Comment on the morphology of the erythrocytes.
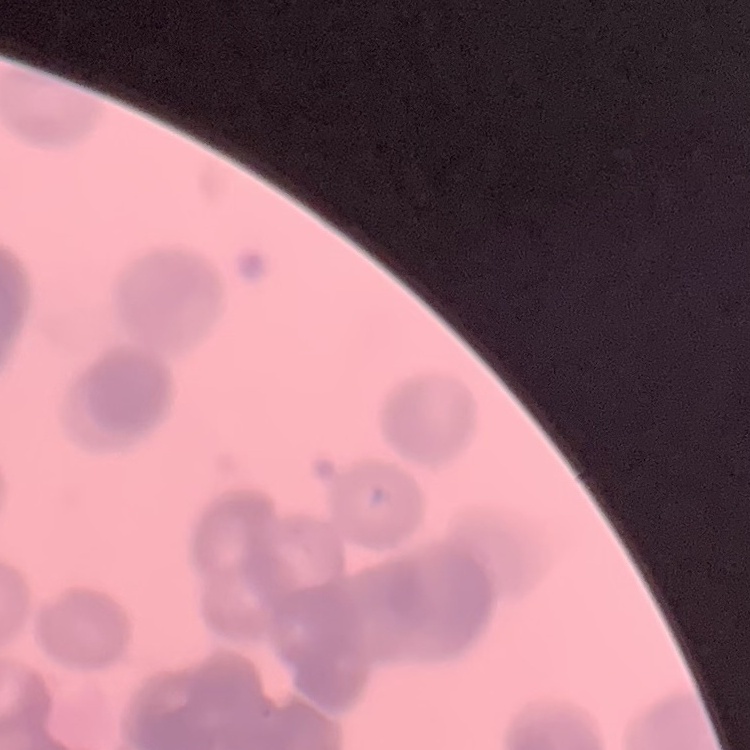
They show rouleaux formation.

stain = Field's or Giemsa
image type = one tile cut from a larger photomicrograph
preparation = thin blood film